Locate and identify every blood parasite.
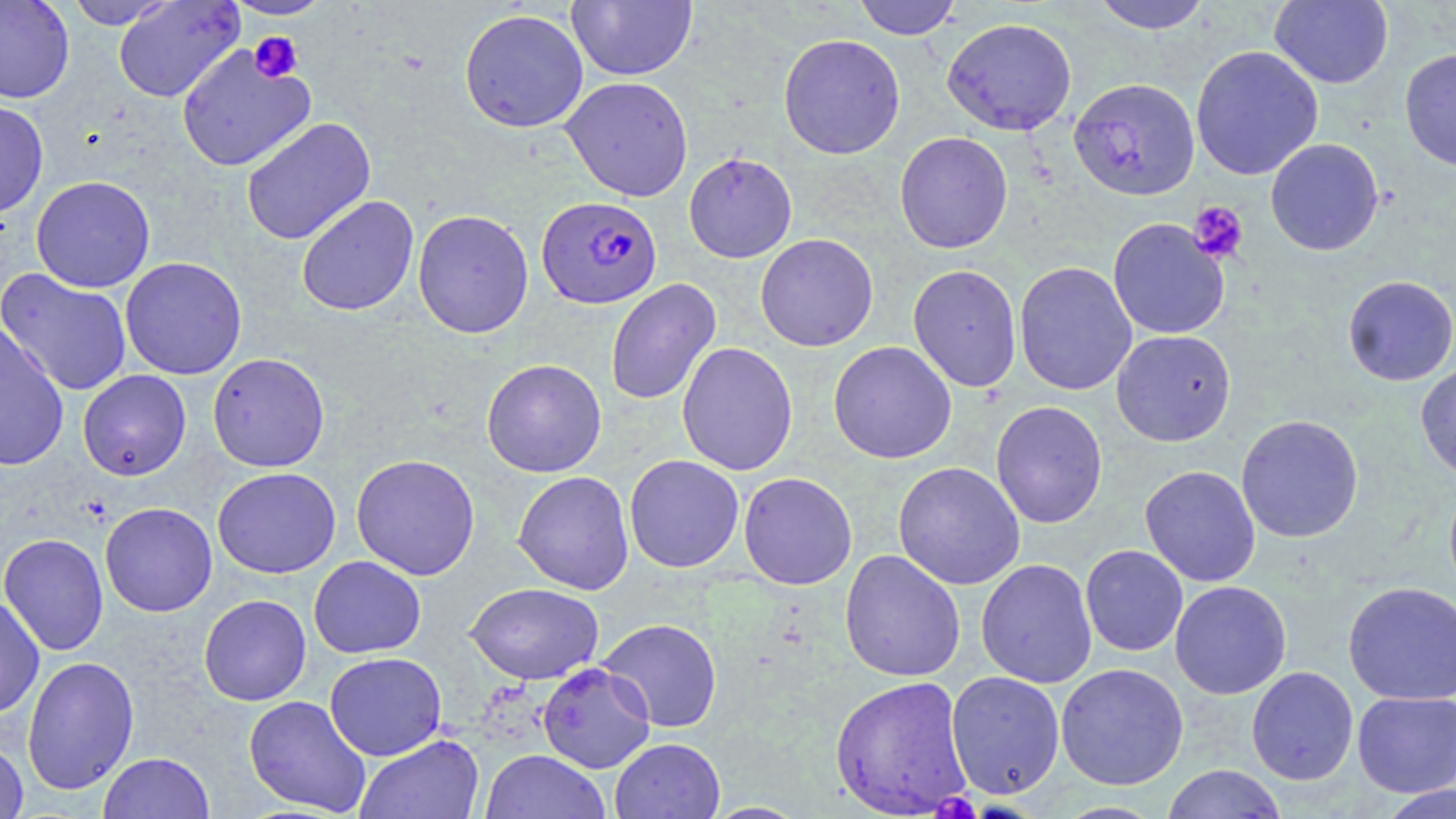

Approximate bounding boxes as named x1/y1/x2/y2 corners in pixels.
Plasmodium falciparum-infected red blood cells: (x1=537, y1=195, x2=661, y2=309).
No Plasmodium ovale, Plasmodium malariae, Plasmodium vivax, Babesia divergens, or Trypanosoma brucei observed.

Uninfected red blood cell locations: (x1=0, y1=0, x2=75, y2=104), (x1=63, y1=0, x2=178, y2=29), (x1=221, y1=0, x2=335, y2=20), (x1=567, y1=0, x2=697, y2=81), (x1=853, y1=0, x2=962, y2=39), (x1=1090, y1=0, x2=1212, y2=33), (x1=1270, y1=0, x2=1393, y2=89), (x1=113, y1=1, x2=245, y2=103), (x1=459, y1=8, x2=589, y2=133), (x1=942, y1=17, x2=1077, y2=136), (x1=778, y1=33, x2=906, y2=160), (x1=176, y1=44, x2=317, y2=172), (x1=1190, y1=45, x2=1323, y2=181), (x1=1399, y1=47, x2=1456, y2=172), (x1=560, y1=76, x2=694, y2=201), (x1=1069, y1=78, x2=1199, y2=200), (x1=0, y1=100, x2=49, y2=220), (x1=241, y1=117, x2=376, y2=245), (x1=894, y1=131, x2=1013, y2=253), (x1=1265, y1=138, x2=1384, y2=256), (x1=683, y1=152, x2=797, y2=263), (x1=31, y1=175, x2=155, y2=293), (x1=296, y1=195, x2=419, y2=316), (x1=412, y1=209, x2=534, y2=339), (x1=1108, y1=218, x2=1230, y2=339), (x1=755, y1=233, x2=878, y2=352), (x1=120, y1=256, x2=247, y2=380), (x1=1014, y1=261, x2=1137, y2=396), (x1=908, y1=264, x2=1022, y2=392), (x1=0, y1=268, x2=133, y2=397), (x1=1342, y1=275, x2=1456, y2=386), (x1=605, y1=278, x2=721, y2=406), (x1=0, y1=322, x2=69, y2=472), (x1=1111, y1=329, x2=1236, y2=446), (x1=677, y1=341, x2=798, y2=476), (x1=828, y1=341, x2=957, y2=464), (x1=207, y1=353, x2=330, y2=472), (x1=481, y1=358, x2=607, y2=478), (x1=1415, y1=362, x2=1456, y2=483), (x1=78, y1=370, x2=191, y2=480), (x1=990, y1=401, x2=1108, y2=528), (x1=1236, y1=414, x2=1363, y2=543), (x1=350, y1=454, x2=480, y2=580), (x1=624, y1=454, x2=744, y2=573), (x1=893, y1=461, x2=1026, y2=590), (x1=1139, y1=465, x2=1261, y2=587), (x1=212, y1=467, x2=341, y2=578), (x1=513, y1=471, x2=635, y2=595), (x1=738, y1=471, x2=857, y2=589), (x1=1444, y1=477, x2=1456, y2=602), (x1=100, y1=502, x2=217, y2=617), (x1=0, y1=533, x2=109, y2=656), (x1=1080, y1=545, x2=1188, y2=657), (x1=839, y1=549, x2=965, y2=682), (x1=308, y1=555, x2=426, y2=658), (x1=976, y1=558, x2=1097, y2=688), (x1=1169, y1=580, x2=1292, y2=699), (x1=464, y1=581, x2=604, y2=684), (x1=1343, y1=581, x2=1456, y2=705), (x1=198, y1=594, x2=311, y2=706), (x1=0, y1=595, x2=45, y2=719), (x1=598, y1=618, x2=723, y2=732), (x1=324, y1=652, x2=447, y2=760), (x1=22, y1=655, x2=140, y2=795), (x1=537, y1=662, x2=656, y2=774), (x1=1055, y1=662, x2=1189, y2=790), (x1=1246, y1=666, x2=1358, y2=785), (x1=945, y1=670, x2=1065, y2=798), (x1=829, y1=675, x2=973, y2=817), (x1=1352, y1=690, x2=1456, y2=797), (x1=243, y1=695, x2=372, y2=816), (x1=355, y1=734, x2=484, y2=819), (x1=0, y1=737, x2=29, y2=819), (x1=610, y1=738, x2=725, y2=819), (x1=480, y1=750, x2=611, y2=819), (x1=98, y1=752, x2=215, y2=819), (x1=1161, y1=764, x2=1288, y2=819), (x1=1377, y1=785, x2=1456, y2=818). Platelet locations: (x1=248, y1=31, x2=304, y2=82), (x1=1189, y1=201, x2=1248, y2=264), (x1=931, y1=794, x2=981, y2=819). Slide-level diagnosis: Plasmodium falciparum. Image is 1456×819 pixels. 1000x magnification. Thin blood smear. Optical microscopy. May-Grünwald-Giemsa stain. One field of a larger specimen.